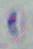
Captured at 1000x magnification. Photomicrograph. Toxoplasma gondii is seen.